Report the malaria status of this cell.
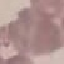

Uninfected.

Summary:
  - Preparation: thin smear
  - Image type: automatically extracted cell patch, resized to 64 × 64 pixels
  - Capture: smartphone through the microscope eyepiece
  - Stain: Giemsa